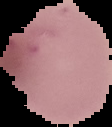

{
  "preparation": "thin blood film",
  "result": "no Plasmodium parasites detected",
  "image_type": "segmented cell region with the area outside set to black",
  "image_size": "112×127 pixels"
}